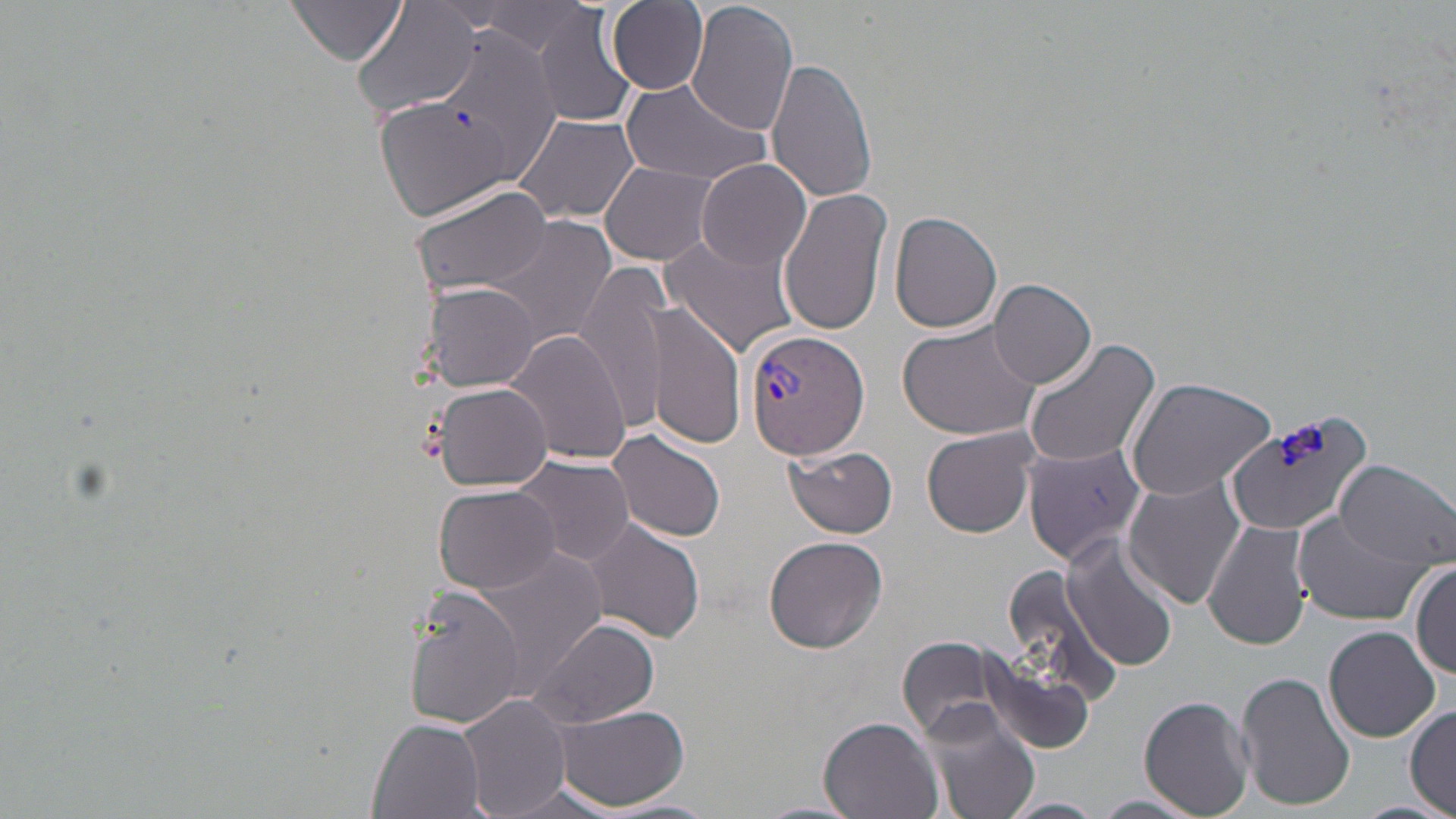

plasmodium_vivax_infected_red_blood_cell_locations: 'approximate bounding boxes as (x1, y1, x2, y2) in pixels: (742, 329, 872, 461)'
slide_level_diagnosis: Plasmodium vivax
modality: light microscopy
image_size: 1456×819 pixels
uninfected_red_blood_cell_locations: 'approximate bounding boxes as (x1, y1, x2, y2) in pixels: (482, 0, 592, 55), (685, 0, 798, 138), (532, 1, 638, 130), (606, 1, 709, 94), (285, 2, 406, 66), (353, 2, 483, 119), (437, 30, 555, 180), (765, 58, 877, 203), (621, 78, 774, 186), (376, 96, 518, 223), (512, 111, 639, 225), (696, 158, 809, 272), (601, 161, 720, 267), (410, 182, 550, 300), (777, 187, 891, 335), (888, 210, 1003, 334), (487, 216, 618, 349), (660, 233, 799, 357), (574, 260, 673, 431), (988, 277, 1097, 389), (420, 281, 544, 391), (645, 301, 746, 451), (898, 316, 1044, 441), (505, 329, 631, 465), (1022, 337, 1160, 470), (1125, 376, 1277, 501), (431, 382, 555, 492), (1225, 406, 1377, 535), (923, 428, 1037, 537), (607, 429, 727, 542), (1023, 440, 1147, 566), (784, 444, 898, 538), (511, 454, 635, 565), (1333, 459, 1456, 571), (1122, 472, 1246, 611), (433, 484, 564, 596), (1292, 507, 1431, 625), (1204, 519, 1313, 650), (586, 520, 704, 642), (763, 534, 889, 654), (1062, 536, 1180, 672), (471, 546, 608, 694), (1411, 561, 1456, 679), (996, 562, 1123, 710), (406, 588, 528, 728), (527, 617, 660, 729), (1323, 626, 1440, 742), (897, 638, 1005, 742), (976, 648, 1104, 756), (1236, 672, 1356, 811), (457, 694, 572, 819), (1140, 694, 1255, 817), (917, 698, 1042, 819), (549, 703, 690, 812), (1404, 705, 1456, 816), (819, 714, 943, 819), (368, 715, 489, 819), (1089, 794, 1204, 819), (1000, 796, 1105, 819)'
magnification: 1000x
field_of_view: single
stain: May-Grünwald-Giemsa
preparation: thin blood film
platelet_locations: 'approximate bounding boxes as (x1, y1, x2, y2) in pixels: (1277, 424, 1331, 469)'